Identify the parasite.
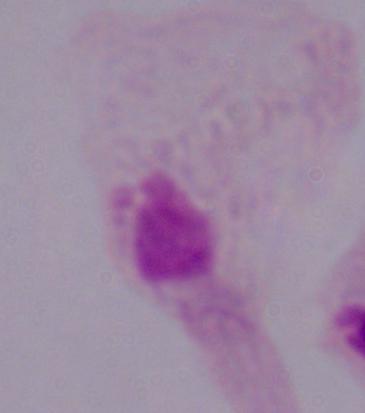
This is a trichomonad.

1000x magnification. Photomicrograph.